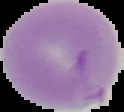

image type = segmented cell region with the area outside set to black
image size = 124×112 pixels
preparation = thin blood film
result = Plasmodium parasites identified